State which parasite is depicted.
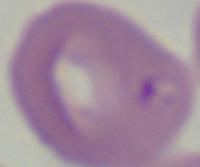
This is Babesia.

modality = photomicrograph
magnification = 1000x